Locate every blood parasite and identify its species.
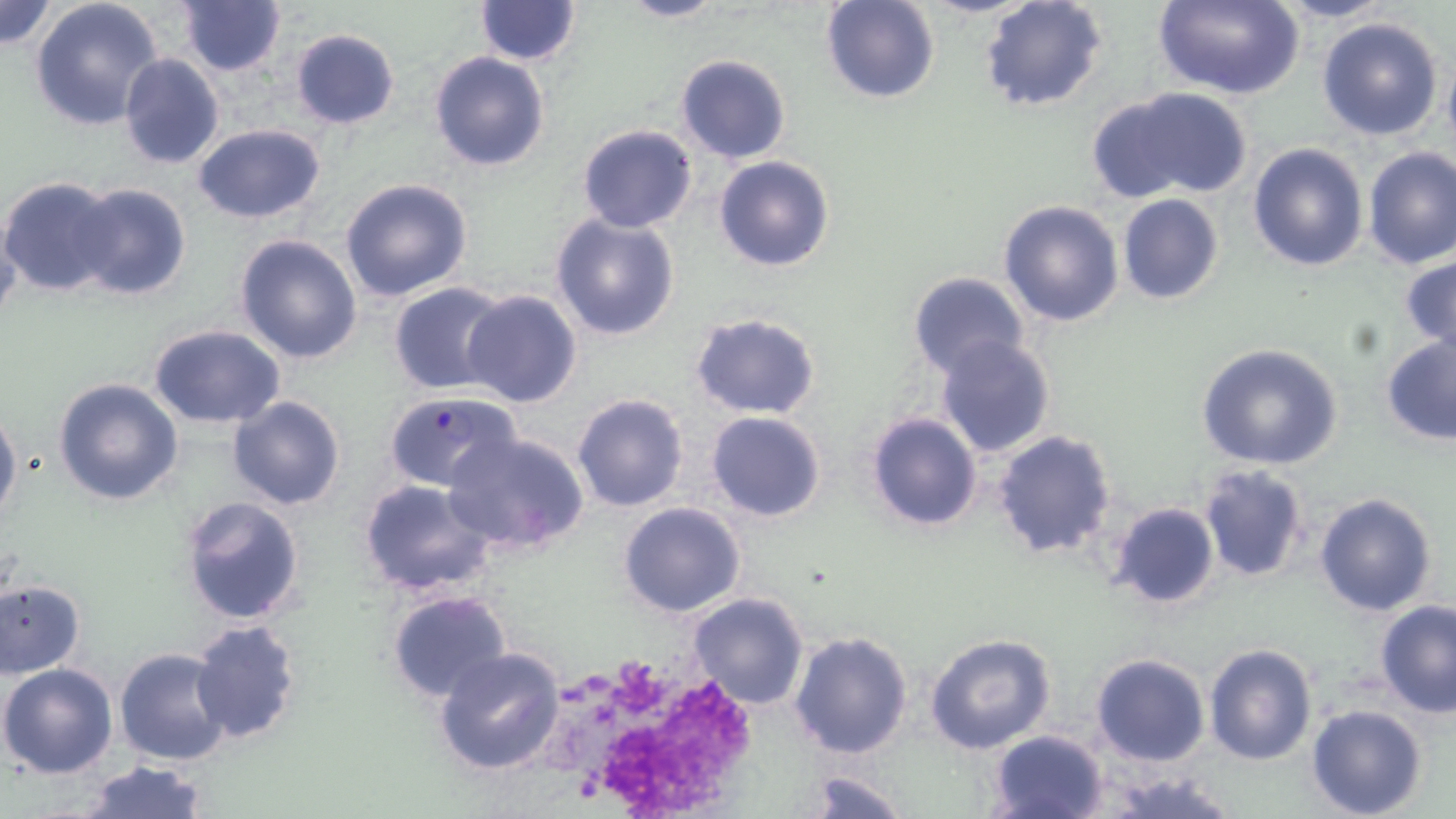

Approximate bounding boxes as named x1/y1/x2/y2 corners in pixels.
Plasmodium falciparum-infected red blood cells: (x1=384, y1=391, x2=520, y2=492).
No Plasmodium ovale, Plasmodium malariae, Plasmodium vivax, Babesia divergens, or Trypanosoma brucei observed.

Summary:
  - White blood cell locations: (x1=526, y1=643, x2=768, y2=812)
  - Uninfected red blood cell locations: (x1=29, y1=0, x2=166, y2=134), (x1=612, y1=0, x2=726, y2=22), (x1=822, y1=0, x2=941, y2=104), (x1=978, y1=0, x2=1108, y2=113), (x1=1150, y1=0, x2=1304, y2=101), (x1=1270, y1=0, x2=1397, y2=23), (x1=0, y1=1, x2=60, y2=55), (x1=176, y1=1, x2=287, y2=78), (x1=474, y1=1, x2=583, y2=65), (x1=1316, y1=15, x2=1445, y2=140), (x1=289, y1=28, x2=401, y2=129), (x1=1442, y1=46, x2=1456, y2=155), (x1=428, y1=50, x2=551, y2=171), (x1=117, y1=53, x2=225, y2=169), (x1=676, y1=53, x2=791, y2=163), (x1=1102, y1=88, x2=1253, y2=201), (x1=193, y1=123, x2=326, y2=222), (x1=577, y1=124, x2=698, y2=233), (x1=1248, y1=142, x2=1369, y2=271), (x1=1362, y1=146, x2=1456, y2=270), (x1=714, y1=156, x2=835, y2=272), (x1=0, y1=177, x2=124, y2=296), (x1=340, y1=177, x2=473, y2=302), (x1=71, y1=182, x2=190, y2=301), (x1=1117, y1=195, x2=1223, y2=306), (x1=998, y1=199, x2=1125, y2=327), (x1=0, y1=213, x2=22, y2=336), (x1=549, y1=213, x2=680, y2=341), (x1=235, y1=233, x2=363, y2=364), (x1=1401, y1=253, x2=1456, y2=354), (x1=908, y1=271, x2=1032, y2=379), (x1=387, y1=281, x2=510, y2=394), (x1=459, y1=290, x2=583, y2=408), (x1=689, y1=313, x2=821, y2=420), (x1=149, y1=324, x2=286, y2=428), (x1=1380, y1=333, x2=1456, y2=446), (x1=935, y1=334, x2=1056, y2=457), (x1=1196, y1=342, x2=1345, y2=469), (x1=53, y1=376, x2=183, y2=506), (x1=571, y1=392, x2=689, y2=513), (x1=226, y1=396, x2=345, y2=510), (x1=0, y1=405, x2=21, y2=526), (x1=706, y1=411, x2=826, y2=522), (x1=866, y1=411, x2=981, y2=532), (x1=444, y1=429, x2=591, y2=556), (x1=992, y1=429, x2=1115, y2=560), (x1=1197, y1=466, x2=1308, y2=583), (x1=358, y1=478, x2=498, y2=595), (x1=1313, y1=491, x2=1438, y2=617), (x1=179, y1=496, x2=307, y2=625), (x1=1106, y1=501, x2=1221, y2=609), (x1=620, y1=503, x2=746, y2=618), (x1=1, y1=579, x2=86, y2=677), (x1=385, y1=589, x2=512, y2=706), (x1=688, y1=593, x2=812, y2=711), (x1=1376, y1=600, x2=1456, y2=717), (x1=189, y1=618, x2=302, y2=742), (x1=789, y1=631, x2=912, y2=758), (x1=926, y1=634, x2=1056, y2=752), (x1=1202, y1=642, x2=1318, y2=767), (x1=114, y1=647, x2=230, y2=766), (x1=433, y1=647, x2=566, y2=776), (x1=1091, y1=654, x2=1211, y2=766), (x1=0, y1=663, x2=119, y2=779), (x1=1307, y1=705, x2=1428, y2=819), (x1=988, y1=729, x2=1110, y2=819), (x1=78, y1=760, x2=213, y2=818), (x1=798, y1=766, x2=912, y2=819), (x1=1089, y1=766, x2=1248, y2=819)
  - Slide-level diagnosis: Plasmodium falciparum
  - Stain: May-Grünwald-Giemsa
  - Preparation: thin blood smear
  - Magnification: 1000x
  - Image size: 1456×819 pixels
  - Field of view: one of a larger specimen
  - Modality: optical microscopy